Describe the morphology of the red blood cells.
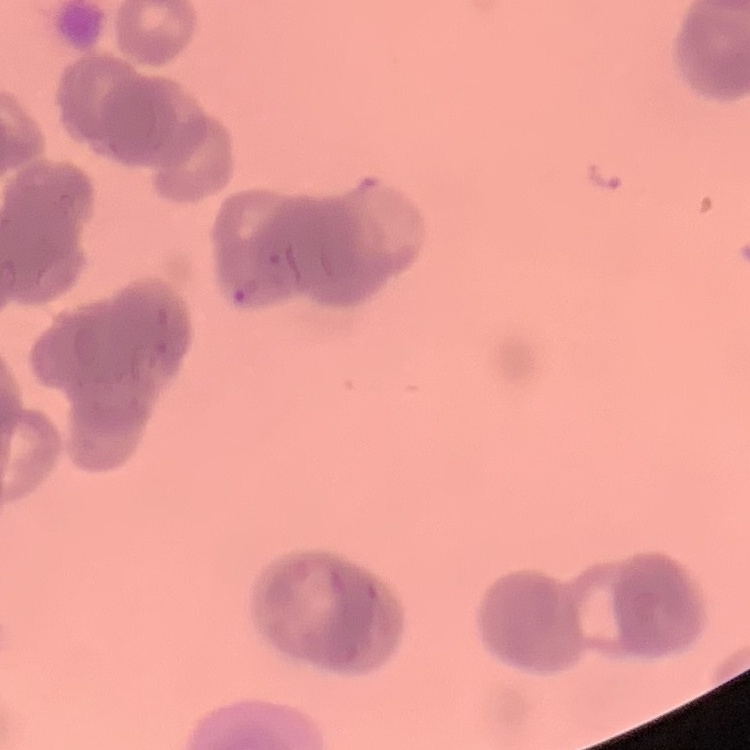
They show rouleaux formation.

{
  "preparation": "thin peripheral smear",
  "image_type": "square crop of a larger photomicrograph",
  "stain": "Field's or Giemsa"
}